Assess the morphology of the erythrocytes.
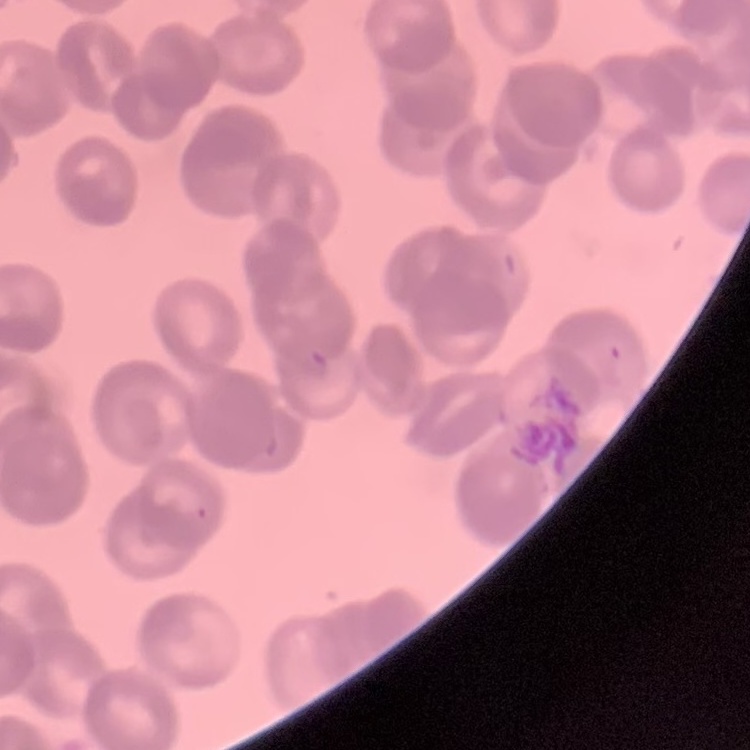
Rouleaux formation.

preparation = thin peripheral smear
image type = square crop of a larger photomicrograph
stain = Field's or Giemsa